Locate and identify every blood parasite.
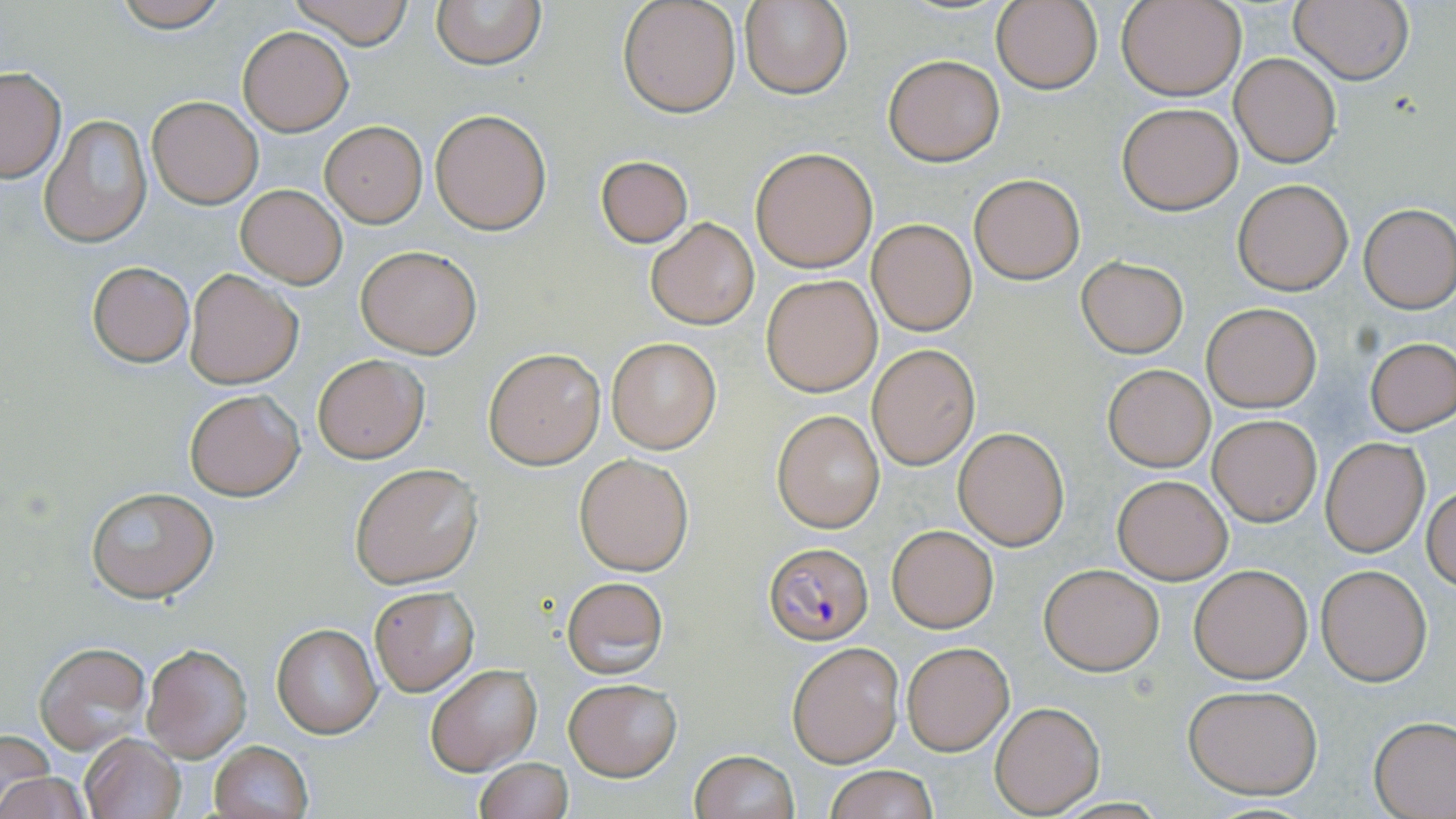

Approximate bounding boxes as (x1, y1, x2, y2) in pixels.
Plasmodium falciparum-infected red blood cells: (764, 541, 874, 646).
No Plasmodium ovale, Plasmodium malariae, Plasmodium vivax, Babesia divergens, or Trypanosoma brucei observed.

Uninfected red blood cell locations: (108, 0, 235, 31), (289, 0, 417, 47), (430, 0, 545, 70), (617, 0, 741, 118), (740, 0, 852, 99), (1118, 0, 1244, 101), (1291, 0, 1414, 86), (991, 1, 1104, 95), (239, 27, 353, 135), (1231, 53, 1340, 166), (882, 55, 1005, 166), (0, 67, 65, 183), (148, 96, 262, 208), (1116, 102, 1241, 214), (430, 109, 552, 235), (41, 114, 155, 248), (320, 121, 427, 227), (750, 147, 878, 272), (594, 155, 693, 247), (969, 173, 1084, 283), (1233, 178, 1354, 295), (235, 183, 348, 288), (1359, 203, 1455, 312), (644, 215, 760, 330), (867, 218, 977, 335), (355, 244, 482, 358), (1076, 255, 1188, 357), (86, 261, 194, 366), (184, 268, 302, 389), (761, 274, 883, 396), (1202, 302, 1321, 412), (1366, 336, 1455, 435), (605, 337, 721, 453), (868, 345, 979, 469), (484, 348, 606, 468), (312, 354, 428, 463), (1103, 365, 1215, 471), (183, 389, 305, 500), (772, 409, 887, 532), (1208, 414, 1322, 526), (953, 426, 1071, 549), (1320, 438, 1429, 556), (574, 454, 693, 575), (349, 462, 482, 588), (1111, 472, 1234, 585), (85, 486, 218, 603), (1424, 486, 1456, 591), (887, 525, 998, 632), (1038, 564, 1164, 675), (1189, 564, 1311, 683), (1316, 565, 1432, 684), (561, 576, 668, 678), (368, 585, 479, 695), (272, 623, 382, 737), (786, 640, 904, 768), (36, 642, 151, 753), (142, 642, 251, 760), (901, 642, 1013, 755), (424, 664, 541, 775), (563, 678, 681, 780), (1182, 683, 1323, 799), (991, 701, 1104, 815), (1370, 717, 1456, 818), (0, 731, 53, 814), (81, 733, 184, 818), (208, 741, 313, 819), (688, 749, 799, 819), (473, 757, 573, 819), (0, 765, 89, 819), (823, 765, 939, 819). Slide-level diagnosis: Plasmodium falciparum. Light microscopy. May-Grünwald-Giemsa stain. Thin blood smear. Captured at 1000x magnification. Single field of view. Image is 1456×819 pixels.